Classify this cell by malaria status.
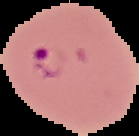
Parasitized.

From a thin blood film. Image is 139×136 pixels. Cell region segmented out of the field of view; the surrounding area is masked to black.